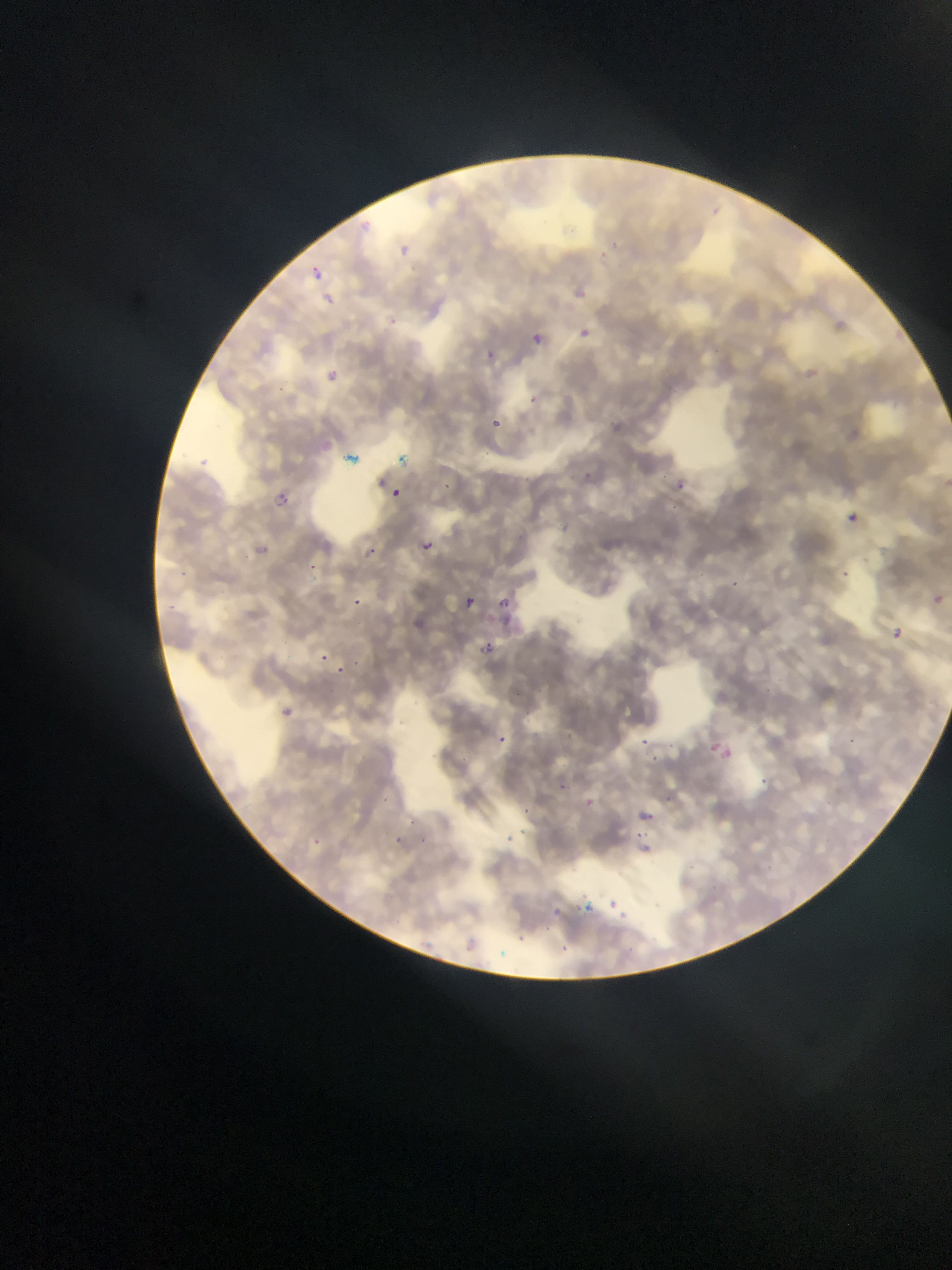
Approximate bounding boxes as [left, top, right, bottom] in pixels.
Summary:
  - Malaria parasite locations: [396, 239, 409, 254], [599, 244, 608, 253], [305, 261, 324, 277], [324, 291, 339, 312], [385, 315, 401, 330], [577, 327, 591, 340], [532, 329, 548, 348], [480, 347, 518, 378], [323, 363, 343, 386], [528, 396, 539, 408], [482, 413, 506, 436], [584, 469, 602, 489], [669, 477, 689, 496], [440, 482, 459, 498], [389, 489, 401, 500], [269, 490, 293, 513], [845, 511, 860, 525], [560, 519, 576, 539], [417, 537, 437, 557], [366, 542, 386, 556], [307, 562, 319, 576], [841, 568, 848, 582], [726, 578, 740, 591], [455, 591, 480, 616], [935, 593, 951, 612], [354, 594, 361, 606], [495, 594, 514, 613], [889, 627, 903, 641], [472, 637, 500, 662], [315, 651, 331, 667], [333, 665, 349, 684], [278, 705, 295, 720], [498, 732, 518, 751], [639, 733, 652, 757], [845, 733, 863, 749], [703, 739, 734, 764], [558, 775, 574, 801], [759, 776, 773, 792], [578, 793, 600, 814], [666, 796, 676, 806], [633, 805, 660, 830], [409, 815, 423, 826], [505, 828, 513, 848], [416, 830, 433, 843], [396, 834, 414, 853], [630, 842, 663, 862], [606, 894, 616, 910], [582, 898, 595, 925], [553, 900, 571, 924], [616, 910, 639, 921], [510, 929, 531, 948], [555, 934, 569, 956]
  - Preparation: thin blood smear
  - Capture: mobile-phone photograph through a microscope
  - Field of view: single
  - Country: Ghana
  - Image size: 952×1270 pixels